Comment on the morphology of the red blood cells.
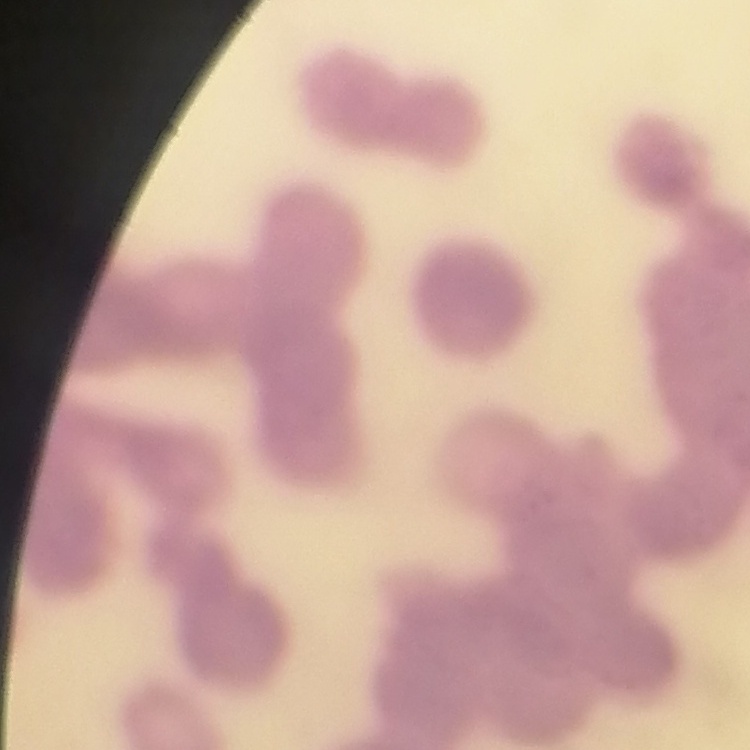

They show rouleaux formation.

Thin blood smear. Stained with either Field's or Giemsa. One tile cut from a larger photomicrograph.